Assess the morphology of the erythrocytes.
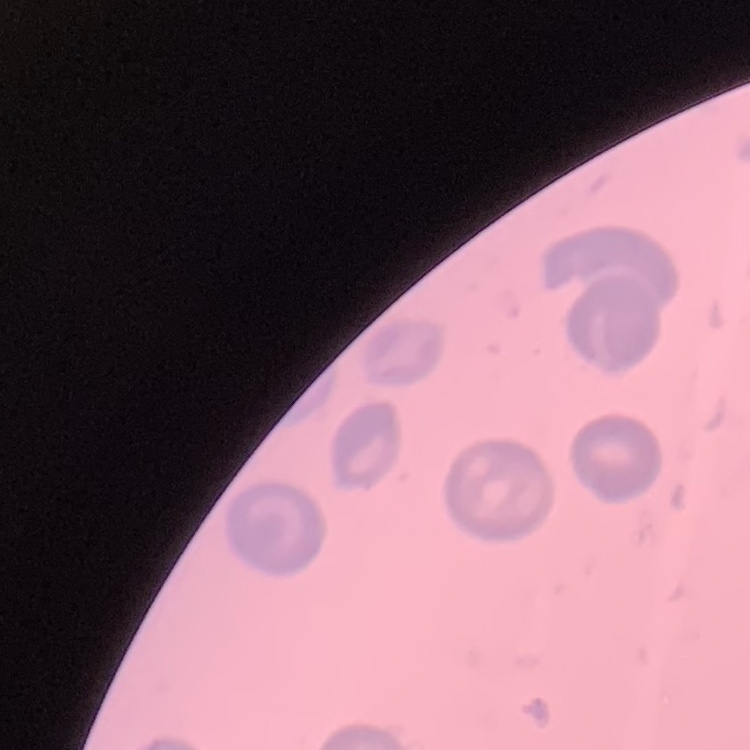
No rouleaux formation.

Field's or Giemsa stain. One tile cut from a larger photomicrograph. Thin blood film.